Assess this cell for malaria.
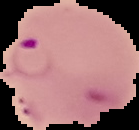

It is parasitized.

Image is 139×130 pixels. From a thin blood smear. The area outside the segmented cell region is set to black.